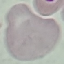
Result: no malaria parasites seen. Thin blood film. Giemsa-stained preparation. Cell patch, automatically extracted from a larger field of view and resized to 64 × 64 pixels. Photographed with a smartphone camera at the microscope eyepiece.